Classify this cell by malaria status.
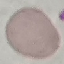
Uninfected.

preparation: thin smear
image_type: automatically extracted cell patch, resized to 64 × 64 pixels
capture: smartphone through the microscope eyepiece
stain: Giemsa